Point out each leukocyte.
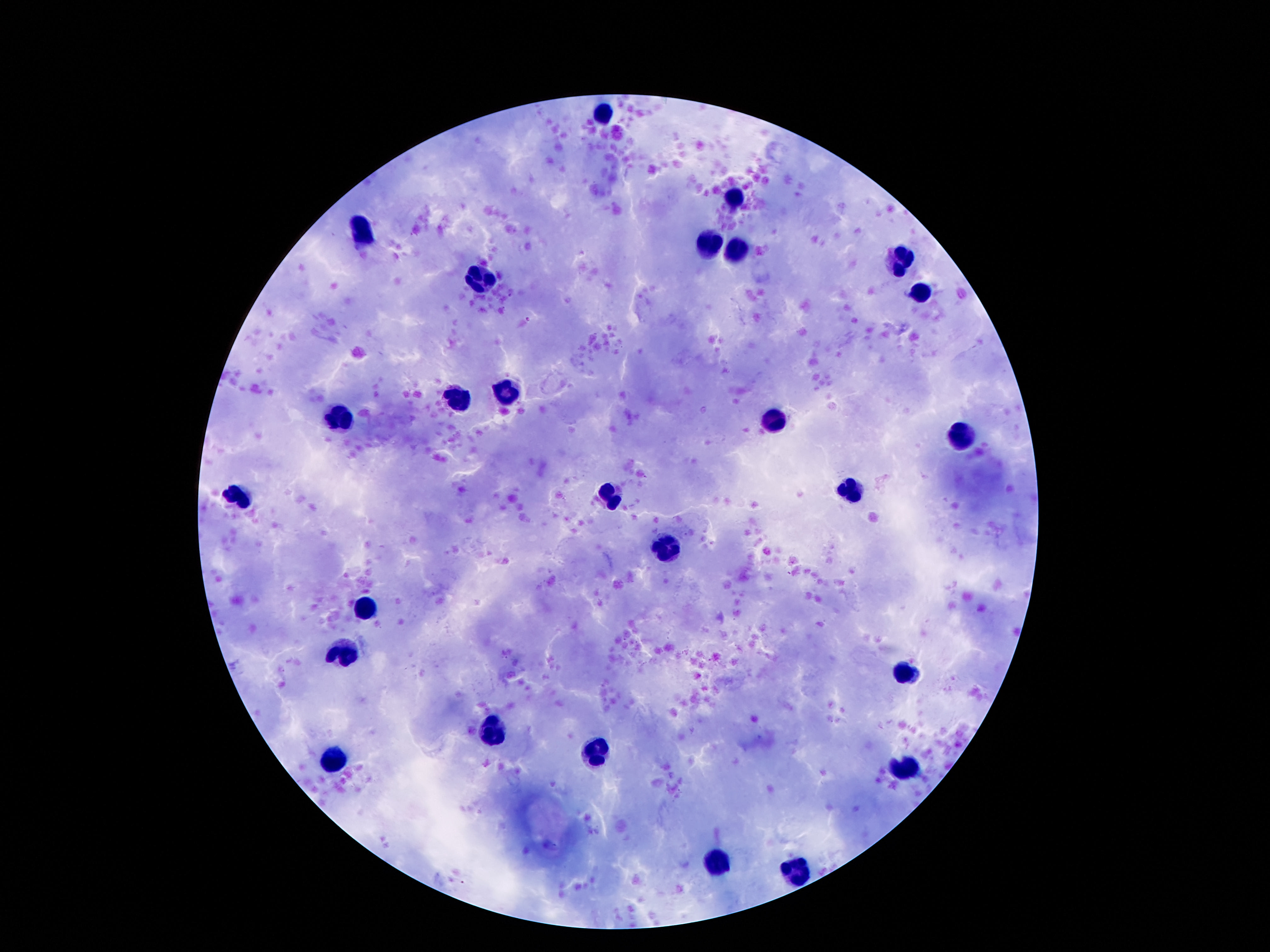

Approximate centers as [x, y] in pixels.
Leukocytes: [605, 110], [737, 201], [363, 230], [710, 242], [745, 247], [901, 263], [483, 278], [922, 289], [506, 392], [458, 396], [340, 418], [773, 421], [962, 432], [851, 490], [613, 495], [237, 497], [666, 547], [363, 609], [344, 651], [907, 674], [496, 731], [599, 751], [336, 760], [909, 767], [714, 863], [800, 872].

100x magnification. Image is 1270×952 pixels. Thick blood smear. Giemsa-stained preparation. Photographed through the microscope eyepiece with a smartphone camera. Patient malaria status: uninfected. Single field of view.